Point out every malaria parasite and every leukocyte.
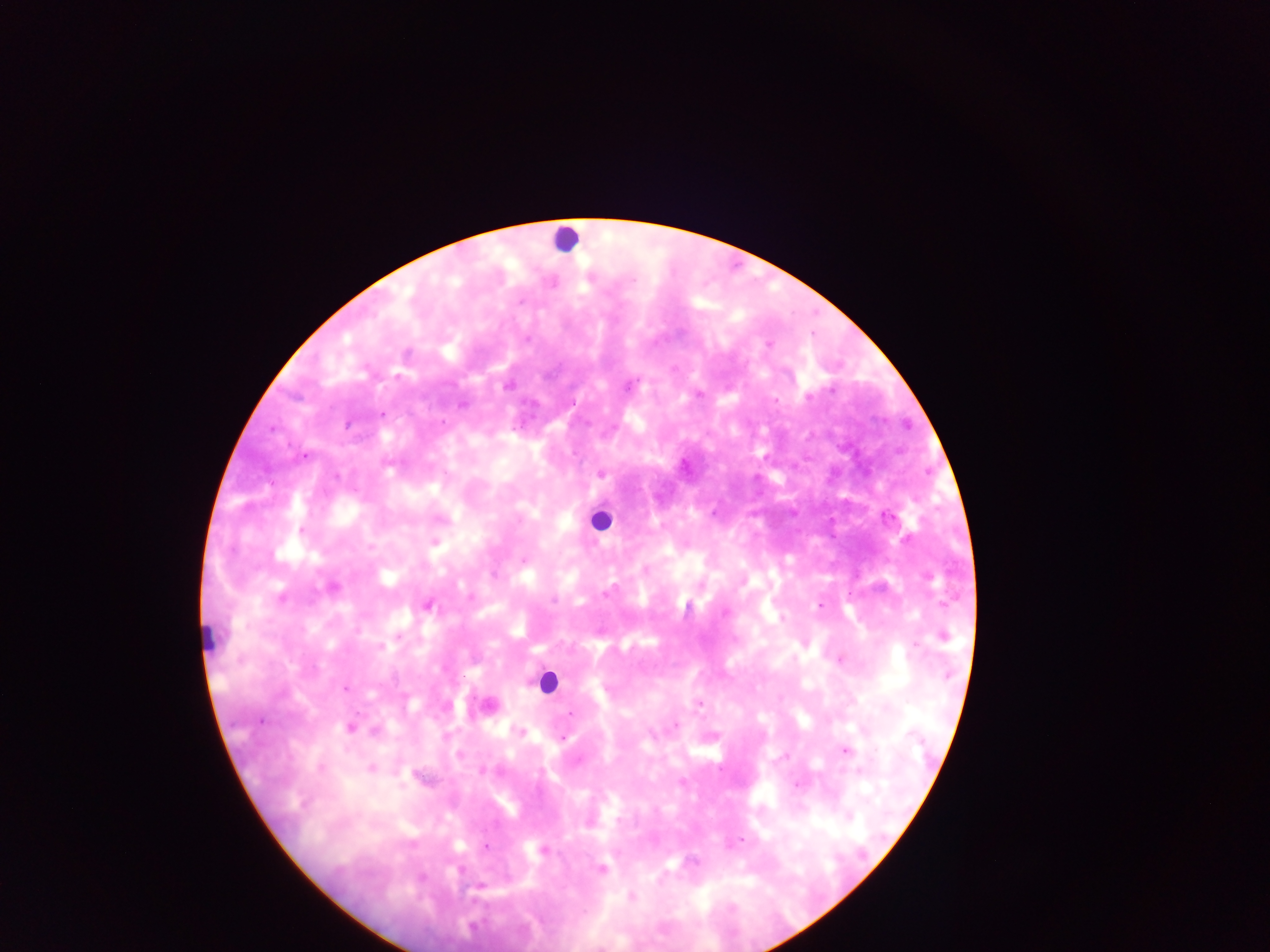
Approximate centers as x y in pixels.
Malaria parasites: 633 280; 520 302; 767 344; 508 386; 808 397; 775 400; 462 405; 382 414; 443 422; 305 457; 683 466; 601 474; 337 476; 301 531; 434 542; 522 560; 607 593; 553 600; 820 605; 428 606; 687 608; 725 612; 781 618; 943 635; 399 636; 915 645; 381 647; 841 660; 947 675; 346 689; 699 703; 571 713; 260 721; 675 725; 350 728; 376 732; 520 732; 564 739; 845 751; 459 755; 785 756; 371 769; 482 771; 797 785; 401 786; 741 840; 486 847; 543 850; 601 869; 632 896.
Leukocytes: 565 238; 599 520; 206 636; 547 681.

Image is 1270×952 pixels. One field of view. Thick blood smear. Photographed through a microscope with a mobile-phone camera. Sample from Ghana.